Give a bounding box for every parasitised red blood cell, every trophozoite, every gametocyte, every leukocyte, and every artifact (platelet-like body, stain precipitate, or debris).
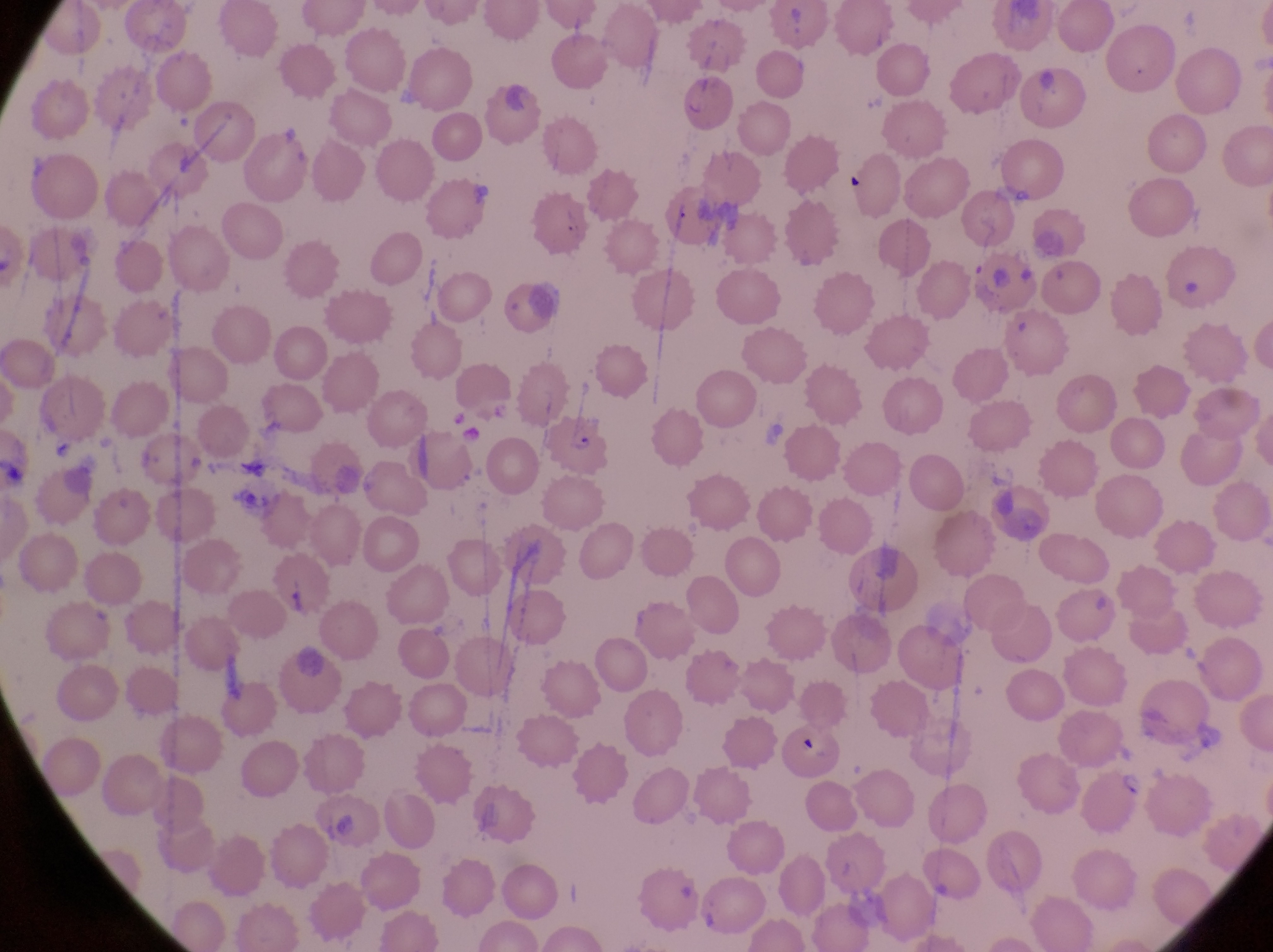
Approximate bounding boxes as {left, top, right, bottom} in pixels.
Parasitised red blood cells: {543, 418, 612, 475}, {1083, 764, 1146, 831}.
No leukocytes observed.
Artifacts (platelet-like body, stain precipitate, or debris): {1180, 275, 1205, 302}, {449, 404, 472, 434}, {329, 807, 361, 842}.

Photographed through the eyepiece of an Olympus CX-23 microscope with a smartphone camera. Magnification of 1000x. One field of view. Thin blood smear. Collected in Uganda. Image is 1273×952 pixels.